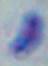

Summary:
  - Modality: micrograph
  - Magnification: 1000x
  - Identification: Toxoplasma gondii